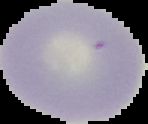

malaria_status: uninfected
preparation: thin blood smear
image_size: 148×124 pixels
image_type: segmented cell region on a black background